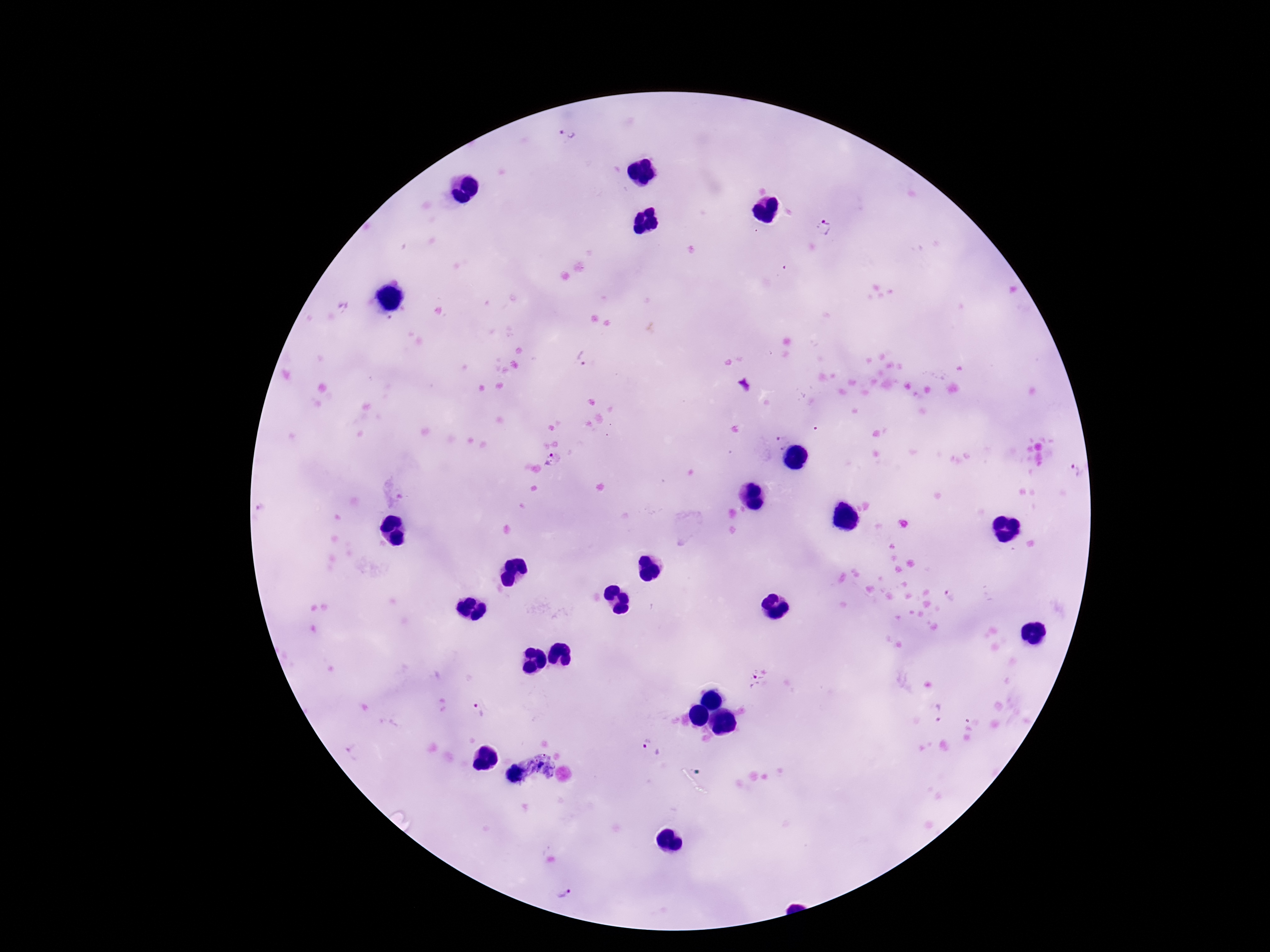

Approximate centers as (x, y) in pixels.
Summary:
  - Plasmodium parasite locations: (570, 132), (825, 226), (583, 359), (782, 442), (552, 460), (1074, 471), (952, 596), (758, 677), (942, 711), (478, 713), (649, 748), (542, 757), (527, 768), (540, 768), (548, 770), (563, 893)
  - Field of view: one from this slide
  - Preparation: thick peripheral-blood smear
  - Stain: Giemsa
  - Patient malaria status: positive
  - Magnification: 100x
  - Capture: smartphone camera through the microscope eyepiece
  - Image size: 1270×952 pixels